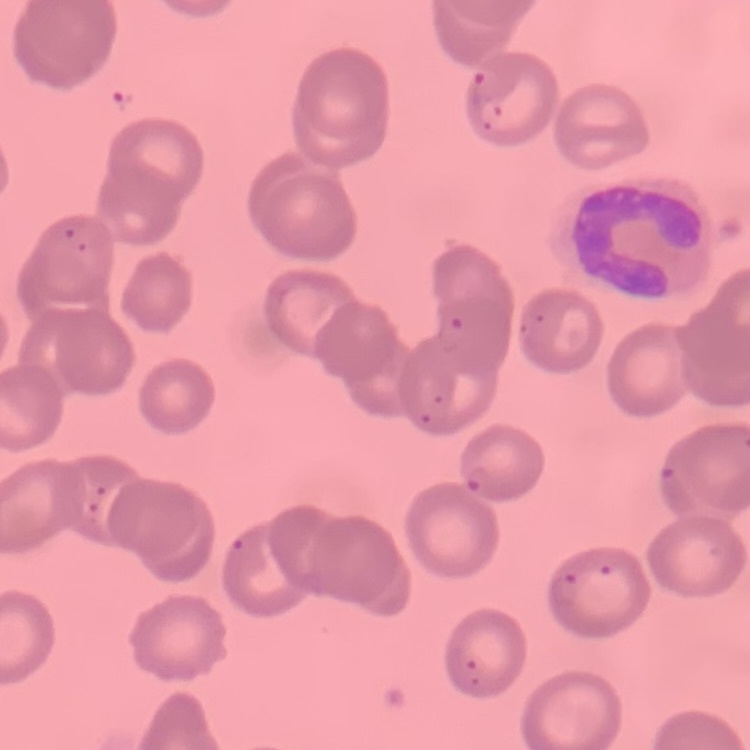
Summary:
  - Red blood cell morphology: no rouleaux formation
  - Image type: square crop of a larger photomicrograph
  - Preparation: thin blood smear
  - Stain: Field's or Giemsa